Assess this cell for malaria.
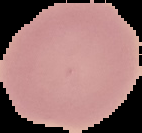
It is uninfected.

Image is 142×133 pixels. From a thin blood smear. Cell region segmented out of the field of view; the surrounding area is masked to black.